Report the malaria status of this cell.
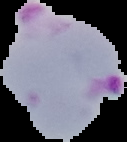
It is parasitized.

Summary:
  - Image size: 127×142 pixels
  - Preparation: thin blood film
  - Image type: cell region segmented out of the field of view; surrounding area masked to black